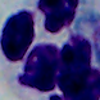
Summary:
  - Identification: white blood cell
  - Modality: micrograph
  - Magnification: 1000x